Assess this cell for malaria.
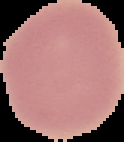

Uninfected.

Image is 124×142 pixels. Segmented cell region on a black background. From a thin blood smear.